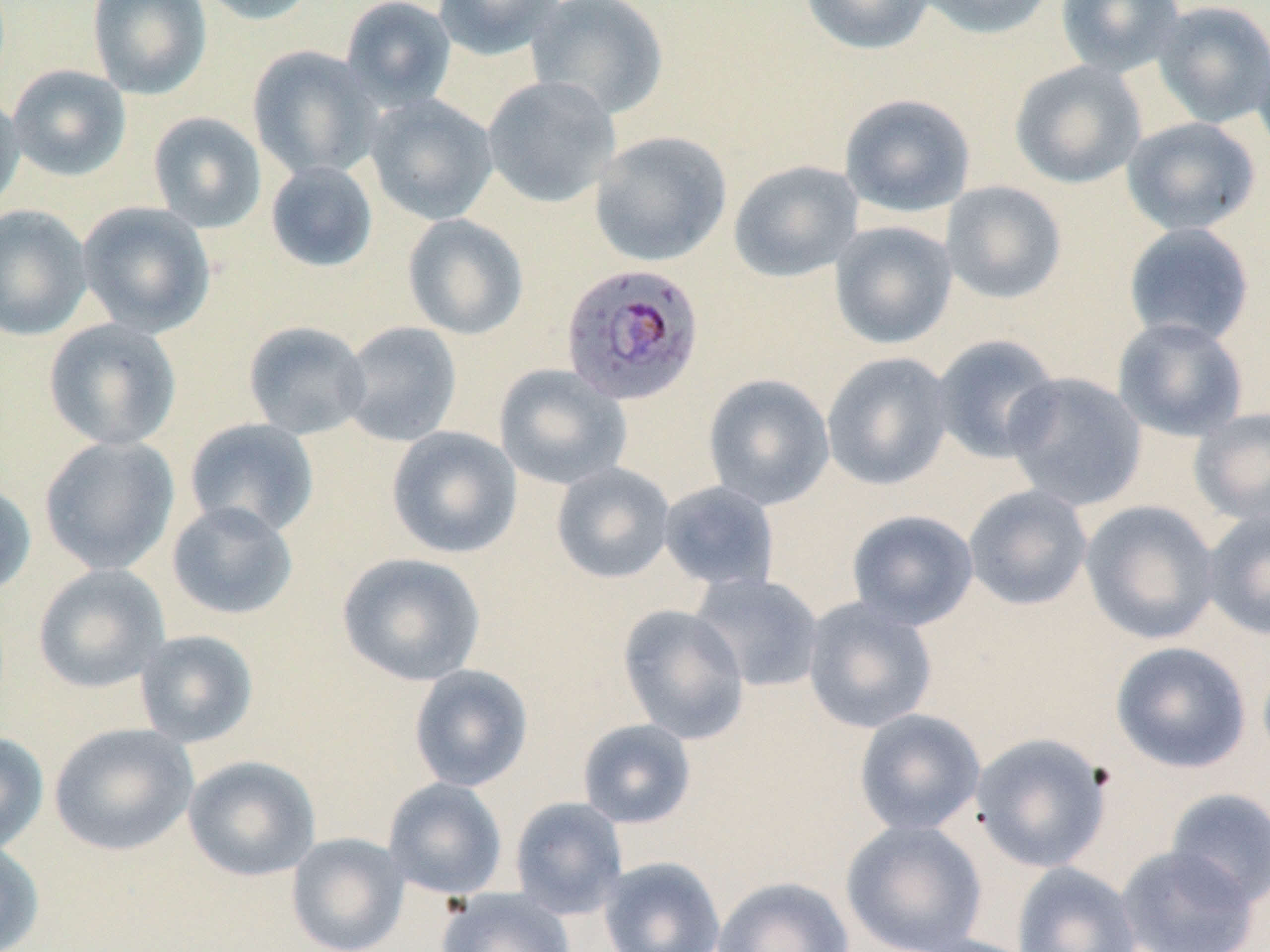

{
  "slide_level_diagnosis": "Plasmodium falciparum",
  "modality": "optical microscopy",
  "plasmodium_falciparum_infected_red_blood_cell_locations": "approximate bounding boxes as [x1, y1, x2, y2] in pixels: [560, 261, 705, 405]",
  "preparation": "thin blood smear",
  "magnification": "1000x",
  "stain": "May-Grünwald-Giemsa",
  "field_of_view": "single",
  "uninfected_red_blood_cell_locations": "approximate bounding boxes as [x1, y1, x2, y2] in pixels: [87, 0, 213, 99], [195, 0, 319, 25], [340, 0, 457, 111], [433, 0, 567, 60], [525, 0, 669, 120], [800, 0, 935, 55], [915, 0, 1058, 39], [1056, 0, 1185, 77], [1152, 0, 1270, 128], [1252, 35, 1270, 158], [247, 45, 382, 181], [1009, 60, 1147, 189], [7, 65, 131, 181], [482, 75, 621, 208], [0, 89, 25, 214], [839, 93, 975, 218], [365, 94, 498, 225], [147, 111, 267, 233], [1121, 117, 1261, 236], [589, 131, 732, 267], [729, 160, 863, 282], [265, 161, 379, 273], [939, 180, 1068, 305], [77, 202, 216, 337], [0, 204, 93, 341], [402, 213, 529, 340], [829, 221, 958, 349], [1122, 222, 1256, 347], [1112, 317, 1248, 442], [43, 318, 182, 451], [242, 321, 372, 440], [339, 321, 462, 447], [931, 334, 1062, 464], [821, 352, 954, 491], [493, 363, 632, 491], [1003, 372, 1148, 511], [703, 373, 835, 510], [1190, 407, 1270, 526], [183, 418, 319, 539], [386, 426, 522, 559], [38, 435, 180, 576], [551, 462, 676, 584], [0, 479, 36, 598], [658, 481, 779, 591], [963, 484, 1093, 611], [166, 500, 298, 621], [1080, 500, 1221, 645], [846, 509, 979, 630], [1201, 509, 1270, 640], [337, 552, 486, 687], [32, 564, 170, 693], [689, 573, 824, 693], [802, 596, 937, 734], [617, 603, 750, 744], [134, 629, 258, 748], [1110, 641, 1251, 773], [408, 664, 533, 792], [854, 708, 986, 836], [576, 718, 697, 829], [49, 722, 198, 856], [0, 730, 49, 854], [970, 732, 1113, 872], [183, 755, 321, 882], [382, 777, 508, 899], [1164, 788, 1270, 909], [509, 796, 629, 920], [841, 819, 988, 952], [286, 832, 410, 952], [0, 838, 44, 952], [1115, 844, 1259, 952], [598, 856, 726, 952], [1012, 862, 1141, 952], [712, 876, 855, 952], [437, 886, 577, 952], [905, 934, 1041, 952]",
  "image_size": "1270×952 pixels"
}